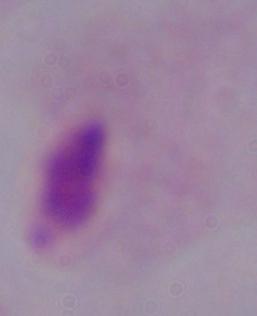

magnification = 1000x
identification = trichomonad
modality = photomicrograph